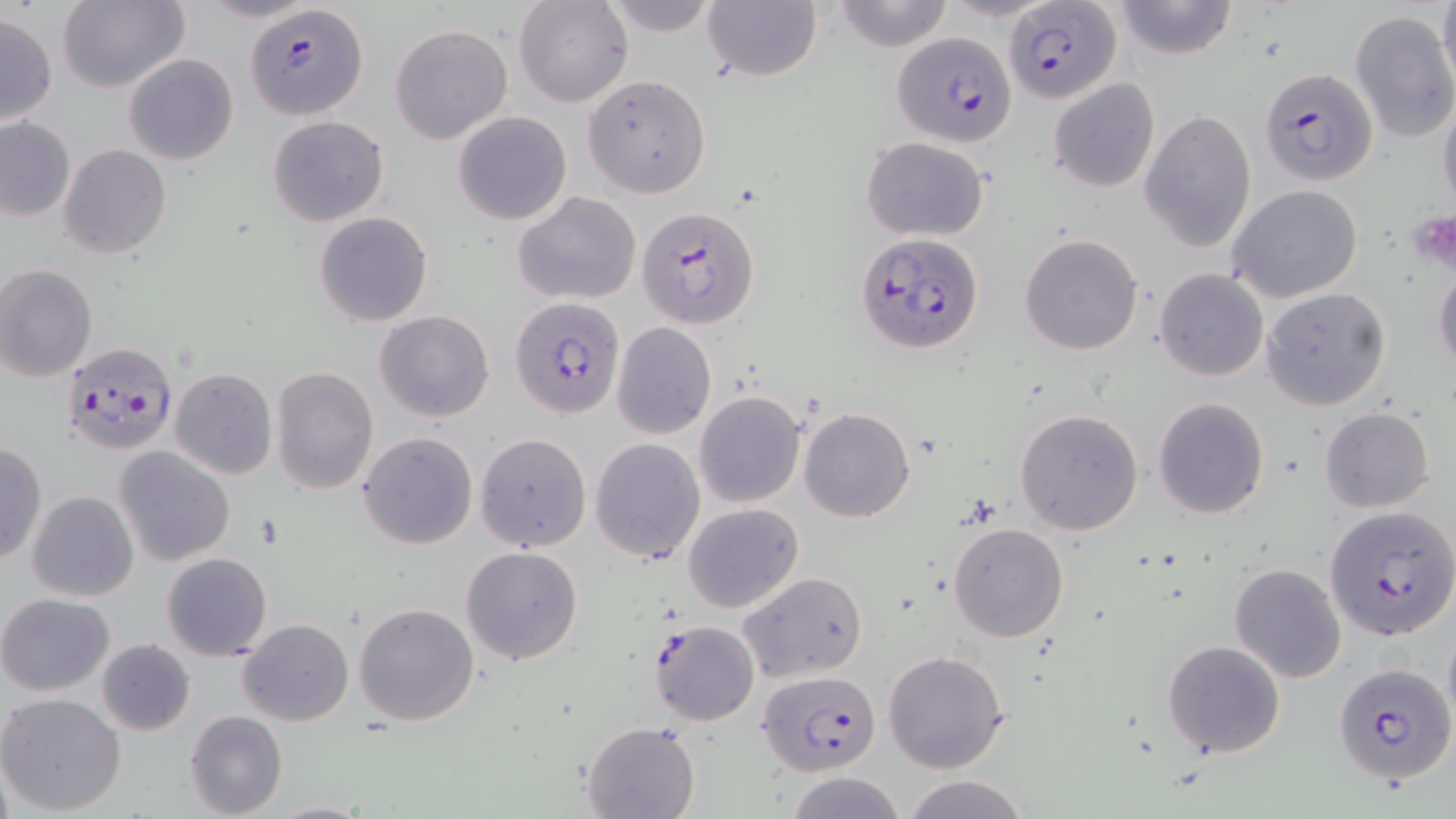 Approximate bounding boxes as [x1, y1, x2, y2] in pixels. Plasmodium falciparum-infected red blood cell locations: [1003, 3, 1119, 106], [247, 5, 367, 122], [892, 34, 1015, 148], [1260, 67, 1379, 186], [638, 205, 761, 329], [855, 232, 985, 356], [510, 295, 624, 418], [62, 342, 180, 456], [1326, 506, 1456, 644], [649, 619, 760, 726], [1332, 661, 1455, 788], [758, 671, 881, 775]. Uninfected red blood cell locations: [56, 0, 189, 92], [198, 0, 319, 24], [600, 0, 722, 36], [831, 0, 955, 52], [941, 0, 1060, 22], [1434, 0, 1455, 91], [513, 1, 633, 107], [702, 1, 823, 84], [1111, 1, 1239, 60], [1349, 10, 1455, 143], [0, 13, 57, 125], [390, 23, 512, 144], [123, 54, 239, 165], [582, 75, 711, 197], [1047, 77, 1160, 192], [1437, 93, 1456, 222], [1140, 109, 1256, 253], [451, 110, 573, 226], [267, 115, 389, 225], [0, 118, 76, 221], [861, 137, 989, 241], [57, 144, 171, 260], [1229, 184, 1363, 303], [513, 192, 641, 304], [314, 211, 433, 326], [1018, 234, 1144, 355], [1432, 258, 1456, 377], [1, 264, 99, 382], [1155, 266, 1269, 381], [1261, 287, 1390, 410], [375, 310, 494, 423], [613, 322, 716, 438], [270, 366, 379, 495], [170, 367, 277, 479], [694, 391, 805, 507], [1153, 397, 1270, 518], [799, 407, 915, 523], [1320, 407, 1434, 512], [1015, 408, 1144, 535], [357, 431, 478, 550], [475, 433, 591, 552], [590, 437, 706, 562], [0, 443, 46, 565], [113, 447, 235, 565], [27, 490, 139, 602], [684, 502, 803, 612], [948, 522, 1069, 642], [460, 546, 583, 664], [161, 551, 272, 660], [1229, 563, 1347, 683], [738, 571, 869, 683], [0, 593, 115, 696], [353, 602, 479, 725], [238, 617, 353, 725], [1443, 622, 1456, 733], [96, 637, 195, 735], [1160, 639, 1285, 758], [881, 649, 1010, 774], [0, 691, 127, 813], [185, 710, 289, 819], [582, 720, 700, 819], [786, 772, 908, 819], [901, 774, 1033, 819], [266, 800, 375, 818]. Slide-level diagnosis: Plasmodium falciparum. May-Grünwald-Giemsa-stained preparation. Optical microscopy. Image is 1456×819 pixels. Single field of view. Thin blood smear. 1000x magnification.